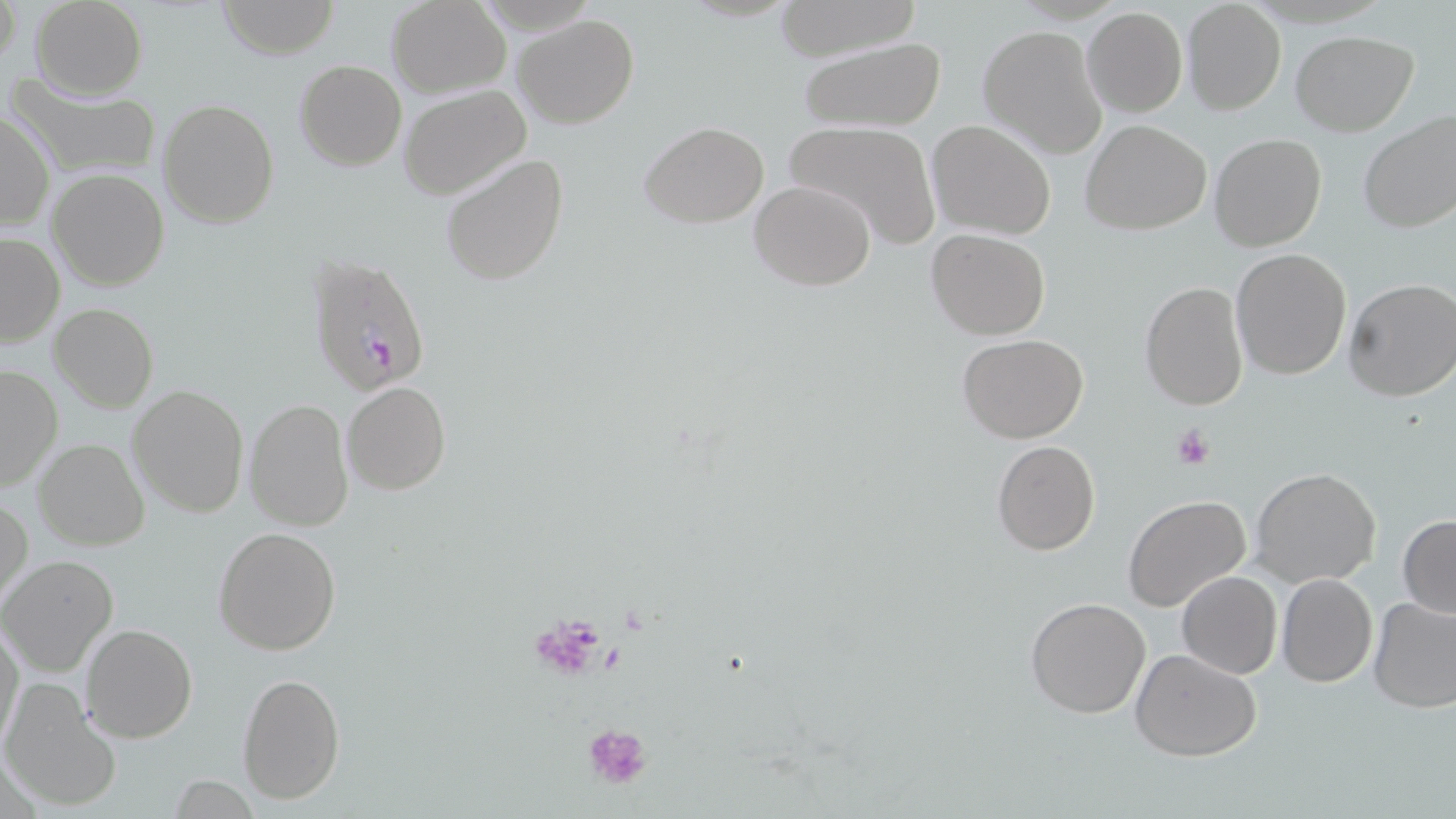

Summary:
  - Coordinate format: approximate bounding boxes as (x1,y1)-(x2,y2) corner pairs in pixels
  - Plasmodium falciparum-infected red blood cell locations: (306,252)-(432,400)
  - Platelet locations: (1172,424)-(1215,470), (581,722)-(653,790)
  - Uninfected red blood cell locations: (0,0)-(20,72), (29,0)-(148,99), (216,0)-(339,58), (387,0)-(509,97), (770,1)-(923,61), (1181,2)-(1286,116), (1083,8)-(1187,118), (512,13)-(639,129), (978,24)-(1107,157), (1290,30)-(1418,136), (796,38)-(946,132), (294,60)-(406,171), (8,75)-(161,181), (400,85)-(531,198), (157,98)-(278,228), (1357,109)-(1456,235), (1,110)-(55,231), (784,119)-(944,249), (927,119)-(1056,240), (1081,119)-(1211,235), (639,121)-(769,228), (1209,133)-(1327,253), (440,152)-(569,286), (46,168)-(169,291), (749,178)-(876,291), (926,229)-(1050,340), (0,232)-(64,348), (1230,248)-(1353,380), (1344,278)-(1456,402), (1139,281)-(1250,411), (48,303)-(159,414), (956,333)-(1089,442), (0,364)-(62,494), (341,381)-(450,496), (127,384)-(250,519), (244,398)-(354,532), (34,438)-(148,552), (991,439)-(1101,555), (1250,467)-(1382,590), (1,493)-(32,608), (1121,494)-(1252,614), (1398,514)-(1456,619), (213,526)-(341,655), (0,554)-(118,677), (1176,570)-(1283,679), (1277,573)-(1378,687), (1367,595)-(1456,712), (1024,598)-(1151,719), (0,623)-(24,749), (81,624)-(197,743), (1130,648)-(1262,763), (236,671)-(346,804), (1,679)-(121,812), (166,776)-(260,817)
  - Slide-level diagnosis: Plasmodium falciparum
  - Magnification: 1000x
  - Field of view: one of a larger specimen
  - Preparation: thin blood smear
  - Modality: optical microscopy
  - Stain: May-Grünwald-Giemsa
  - Image size: 1456×819 pixels